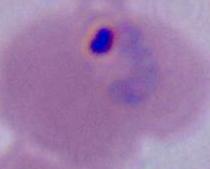
{
  "modality": "micrograph",
  "identification": "Plasmodium",
  "magnification": "400x or 1000x"
}